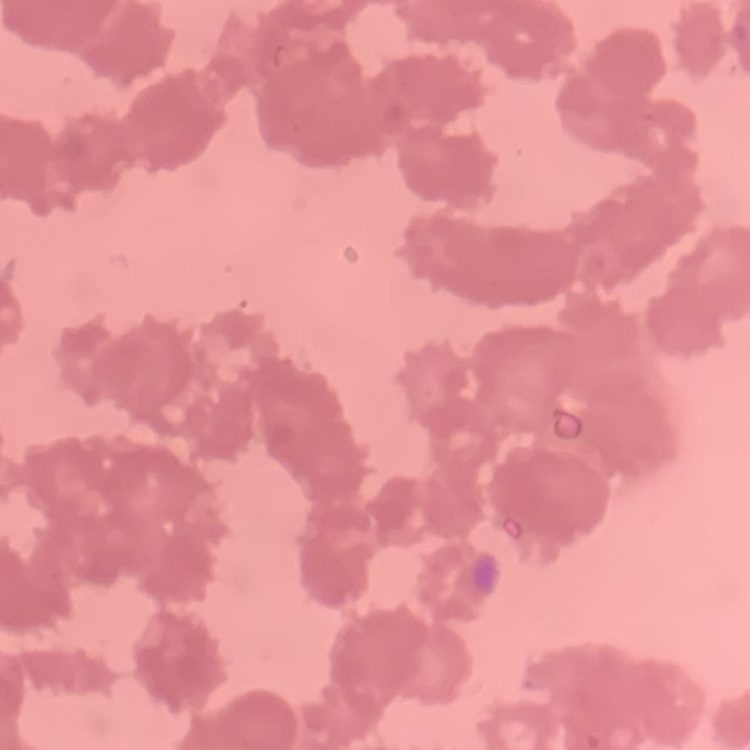
Summary:
  - Red blood cell morphology: rouleaux formation
  - Preparation: thin blood smear
  - Image type: square crop of a larger photomicrograph
  - Stain: Field's or Giemsa